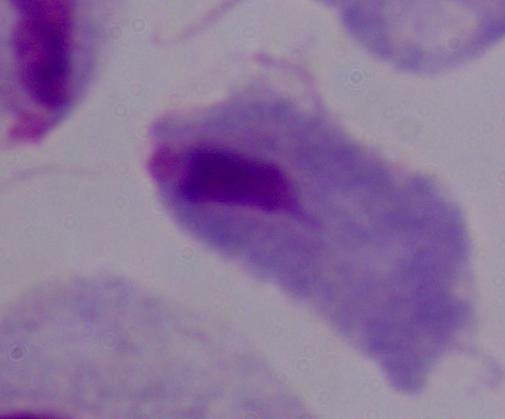

Summary:
  - Magnification: 1000x
  - Identification: trichomonad
  - Modality: photomicrograph